Describe the morphology of the red blood cells.
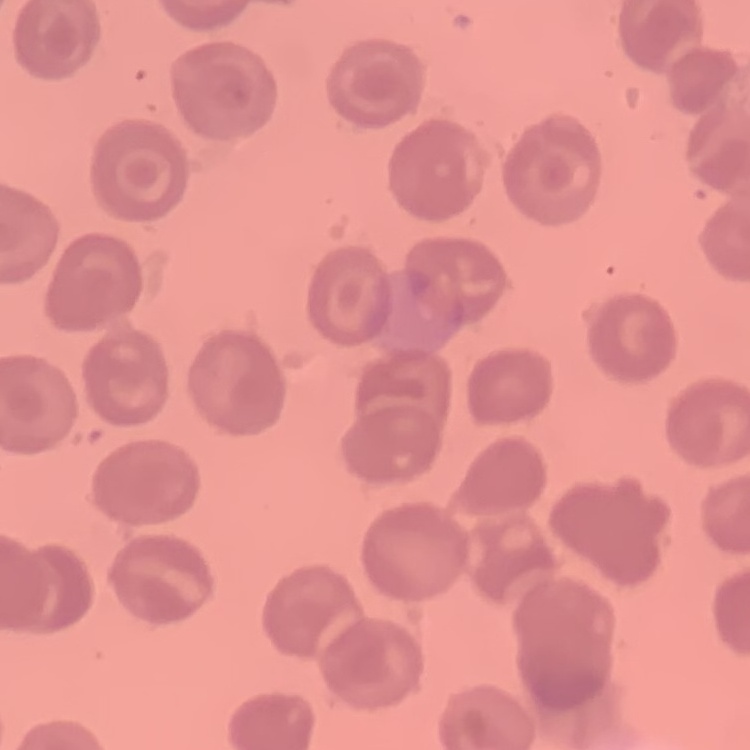

No rouleaux formation.

image type = square crop of a larger photomicrograph
stain = Field's or Giemsa
preparation = thin blood film